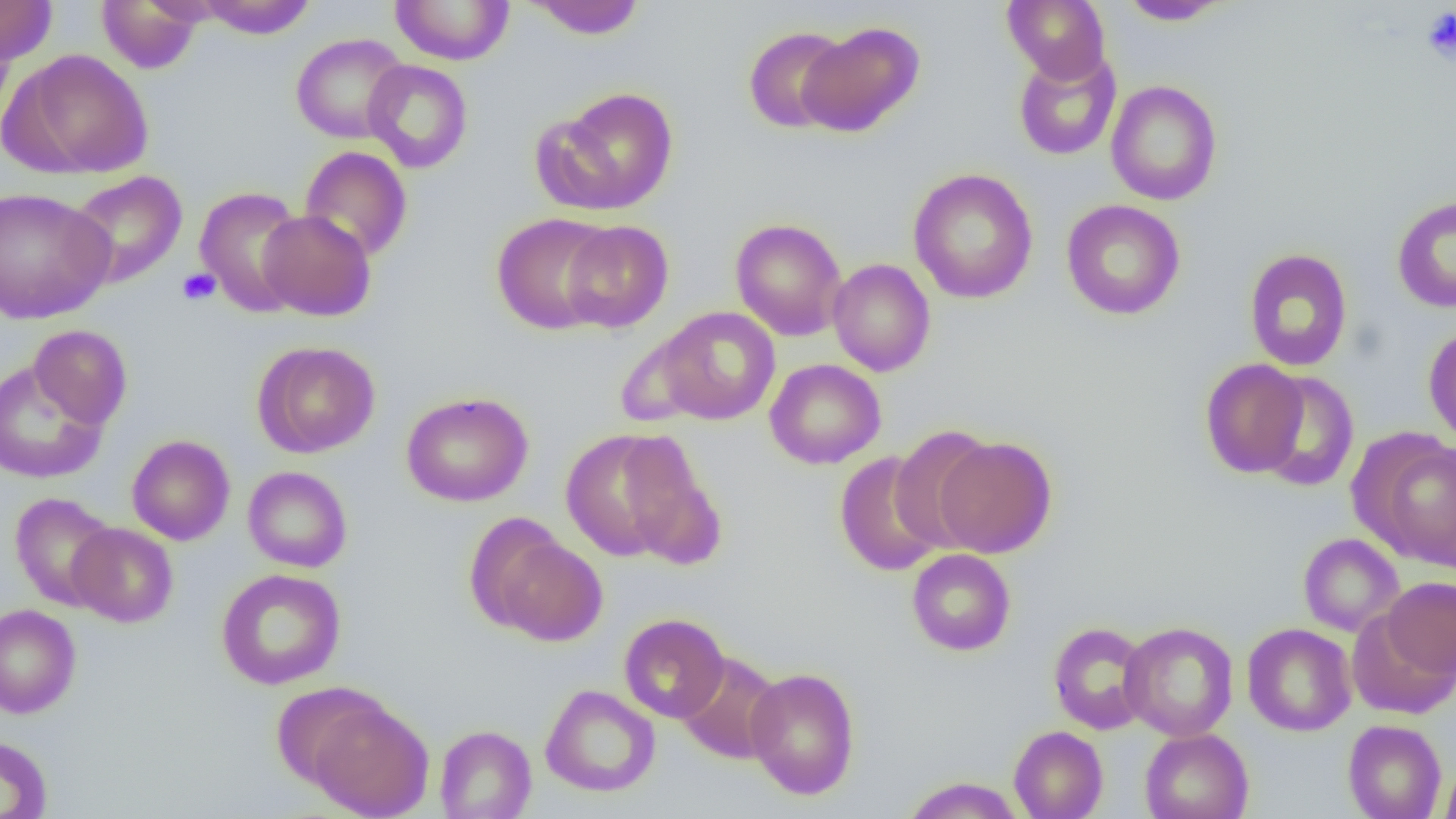
Summary:
  - Coordinate format: approximate bounding boxes as (x1, y1, x2, y2) in pixels
  - Uninfected red blood cell locations: (0, 0, 57, 65), (390, 0, 514, 65), (526, 0, 647, 39), (1002, 0, 1111, 83), (1117, 0, 1232, 26), (96, 1, 204, 74), (195, 1, 318, 38), (0, 16, 16, 128), (797, 21, 925, 137), (743, 26, 851, 133), (290, 33, 409, 144), (1012, 47, 1122, 161), (9, 49, 154, 179), (362, 59, 473, 173), (1105, 80, 1223, 205), (544, 86, 680, 215), (299, 146, 413, 262), (908, 168, 1038, 304), (66, 170, 188, 289), (193, 186, 310, 317), (0, 187, 114, 323), (1391, 195, 1456, 313), (1061, 199, 1186, 320), (258, 209, 376, 321), (491, 213, 616, 334), (731, 218, 847, 341), (561, 220, 674, 333), (1244, 248, 1353, 371), (827, 258, 936, 376), (656, 307, 781, 424), (28, 325, 132, 429), (1423, 326, 1456, 446), (252, 340, 380, 458), (765, 359, 886, 469), (1199, 359, 1310, 479), (0, 360, 108, 484), (1254, 371, 1360, 492), (402, 391, 533, 507), (889, 424, 998, 552), (559, 429, 696, 561), (1363, 434, 1455, 569), (126, 435, 235, 545), (933, 435, 1057, 558), (619, 446, 727, 570), (834, 451, 946, 577), (242, 466, 353, 573), (9, 492, 119, 611), (68, 522, 178, 627), (486, 532, 608, 645), (1298, 533, 1404, 636), (906, 549, 1016, 656), (216, 568, 346, 690), (1381, 575, 1456, 679), (0, 604, 81, 718), (618, 614, 730, 723), (1048, 621, 1153, 734), (1120, 621, 1238, 742), (1242, 623, 1357, 737), (675, 652, 784, 764), (744, 667, 860, 800), (270, 680, 390, 791), (540, 684, 661, 797), (308, 698, 434, 818), (1342, 719, 1447, 819), (435, 724, 536, 818), (1008, 726, 1108, 818), (1139, 728, 1254, 819), (0, 735, 53, 819), (1439, 761, 1456, 818), (901, 777, 1025, 818)
  - Platelet locations: (1422, 7, 1456, 63), (178, 268, 220, 306)
  - Slide-level diagnosis: negative for blood parasites
  - Magnification: 1000x
  - Preparation: thin blood smear
  - Modality: light microscopy
  - Image size: 1456×819 pixels
  - Field of view: one of a larger specimen